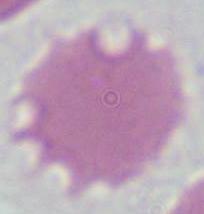

1000x magnification. An erythrocyte is seen. Micrograph.